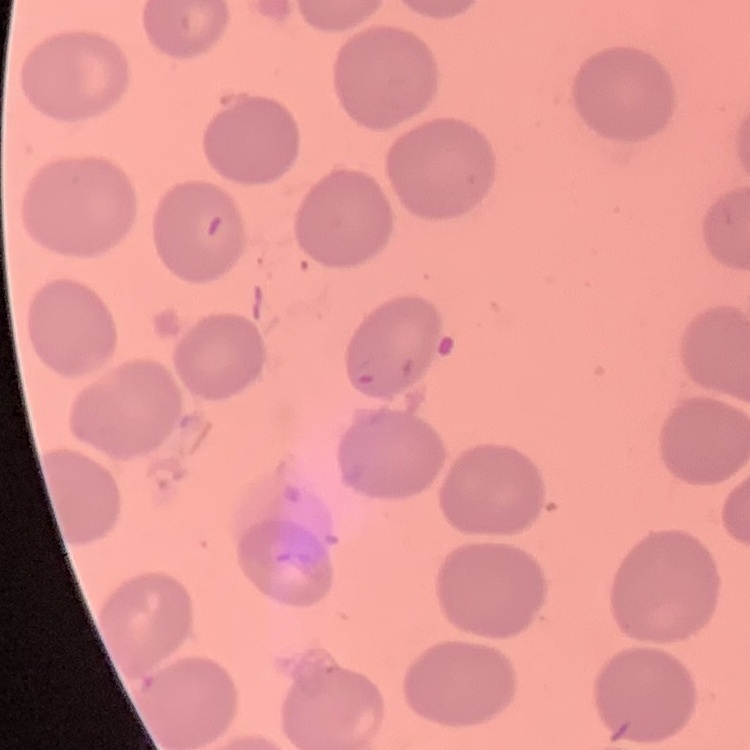
{
  "erythrocyte_morphology": "no rouleaux formation",
  "stain": "Field's or Giemsa",
  "preparation": "thin blood smear",
  "image_type": "square crop of a larger photomicrograph"
}